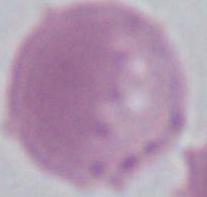

{
  "modality": "photomicrograph",
  "identification": "red blood cell",
  "magnification": "1000x"
}